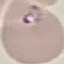

Malaria status: parasitized. Cell patch, automatically extracted from a larger field of view and resized to 64 × 64 pixels. Acquired by smartphone through the microscope eyepiece. Thin blood film. Giemsa stain.